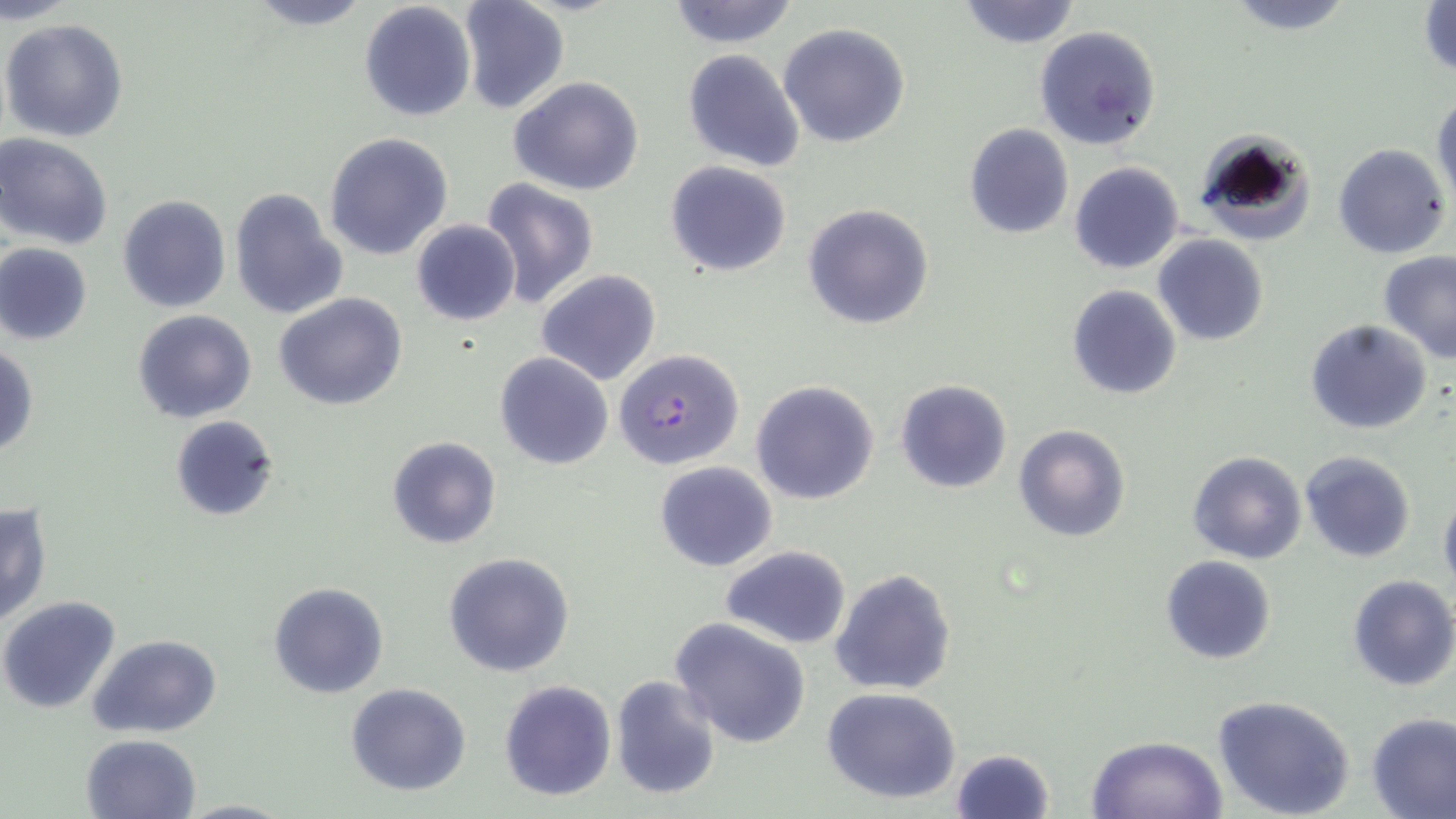
slide-level diagnosis = Plasmodium falciparum
modality = light microscopy
image size = 1456×819 pixels
magnification = 1000x
Plasmodium falciparum-infected red blood cell locations = approximate bounding boxes as (x1, y1, x2, y2) in pixels: (616, 352, 746, 474)
stain = May-Grünwald-Giemsa
preparation = thin blood film
field of view = single
uninfected red blood cell locations = approximate bounding boxes as (x1, y1, x2, y2) in pixels: (457, 0, 570, 117), (665, 0, 801, 49), (955, 0, 1081, 48), (1223, 0, 1358, 36), (359, 1, 477, 123), (236, 2, 378, 31), (1418, 3, 1455, 81), (2, 17, 129, 142), (777, 22, 912, 150), (1033, 24, 1162, 152), (682, 49, 805, 172), (508, 75, 645, 195), (1431, 89, 1455, 213), (964, 124, 1074, 239), (1193, 129, 1315, 247), (323, 132, 453, 260), (0, 133, 113, 250), (1332, 143, 1451, 259), (664, 160, 794, 278), (1069, 162, 1184, 275), (476, 178, 599, 308), (229, 186, 348, 323), (116, 195, 231, 313), (802, 203, 935, 331), (410, 219, 521, 326), (1154, 234, 1270, 345), (0, 244, 93, 345), (1377, 251, 1456, 363), (536, 270, 662, 386), (1065, 286, 1182, 400), (274, 293, 406, 410), (132, 309, 256, 423), (1305, 319, 1433, 435), (1, 342, 38, 458), (494, 352, 617, 472), (750, 379, 880, 505), (894, 379, 1013, 493), (169, 415, 280, 523), (1013, 424, 1130, 541), (386, 435, 502, 549), (1188, 450, 1307, 564), (1300, 450, 1416, 563), (652, 460, 775, 570), (1438, 486, 1456, 594), (1, 502, 52, 626), (720, 545, 851, 648), (443, 552, 576, 678), (1161, 555, 1277, 666), (830, 569, 957, 696), (1346, 574, 1456, 692), (267, 581, 390, 700), (0, 594, 122, 715), (670, 619, 811, 751), (89, 634, 224, 739), (609, 674, 722, 803), (498, 679, 617, 803), (346, 683, 473, 798), (820, 688, 962, 804), (1211, 695, 1357, 819), (1366, 712, 1456, 818), (80, 734, 203, 819), (1084, 735, 1230, 819), (949, 748, 1055, 819), (176, 797, 294, 818)